Assess this cell for malaria.
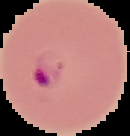
Parasitized.

image type = segmented cell region with the area outside set to black
image size = 130×136 pixels
preparation = thin blood film